Assess this cell for malaria.
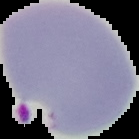
Parasitized.

Image is 139×139 pixels. Cell region segmented out of the field of view; the surrounding area is masked to black. From a thin blood film.